Locate every blood parasite and identify its species.
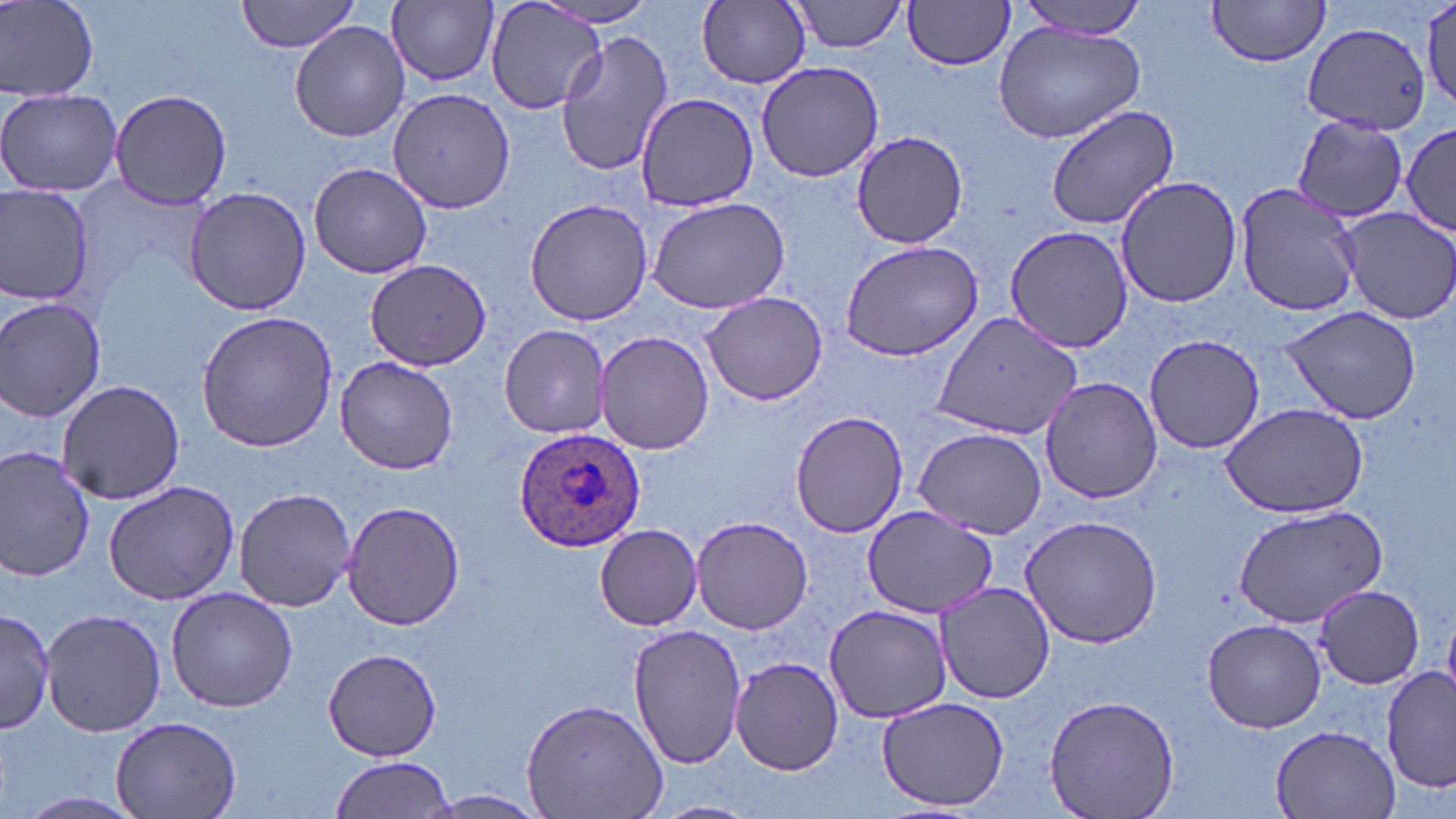
Approximate bounding boxes as named x1/y1/x2/y2 corners in pixels.
Plasmodium ovale-infected red blood cells: (x1=513, y1=426, x2=645, y2=554).
No Plasmodium falciparum, Plasmodium malariae, Plasmodium vivax, Babesia divergens, or Trypanosoma brucei observed.

Summary:
  - Uninfected red blood cell locations: (x1=2, y1=0, x2=98, y2=101), (x1=235, y1=0, x2=366, y2=54), (x1=484, y1=0, x2=607, y2=116), (x1=788, y1=0, x2=909, y2=54), (x1=903, y1=0, x2=1017, y2=71), (x1=1013, y1=0, x2=1153, y2=39), (x1=1206, y1=0, x2=1332, y2=66), (x1=388, y1=1, x2=498, y2=87), (x1=536, y1=1, x2=662, y2=29), (x1=697, y1=2, x2=810, y2=89), (x1=1421, y1=2, x2=1456, y2=110), (x1=290, y1=21, x2=410, y2=143), (x1=994, y1=21, x2=1145, y2=142), (x1=1305, y1=21, x2=1433, y2=133), (x1=554, y1=29, x2=674, y2=179), (x1=757, y1=60, x2=884, y2=184), (x1=388, y1=86, x2=515, y2=212), (x1=0, y1=87, x2=122, y2=198), (x1=108, y1=88, x2=232, y2=208), (x1=634, y1=93, x2=760, y2=211), (x1=1045, y1=103, x2=1181, y2=229), (x1=1292, y1=115, x2=1411, y2=223), (x1=1401, y1=121, x2=1454, y2=241), (x1=848, y1=130, x2=969, y2=248), (x1=307, y1=162, x2=433, y2=278), (x1=1115, y1=175, x2=1243, y2=308), (x1=1235, y1=181, x2=1363, y2=319), (x1=0, y1=183, x2=95, y2=309), (x1=184, y1=185, x2=311, y2=317), (x1=645, y1=195, x2=791, y2=315), (x1=524, y1=198, x2=654, y2=327), (x1=1337, y1=207, x2=1456, y2=324), (x1=1002, y1=224, x2=1136, y2=355), (x1=839, y1=238, x2=986, y2=361), (x1=364, y1=258, x2=491, y2=370), (x1=700, y1=290, x2=831, y2=406), (x1=0, y1=297, x2=106, y2=423), (x1=1280, y1=303, x2=1423, y2=426), (x1=196, y1=309, x2=338, y2=453), (x1=930, y1=310, x2=1082, y2=441), (x1=499, y1=324, x2=614, y2=438), (x1=596, y1=331, x2=714, y2=456), (x1=1142, y1=334, x2=1268, y2=455), (x1=336, y1=356, x2=458, y2=475), (x1=1040, y1=377, x2=1165, y2=503), (x1=57, y1=379, x2=187, y2=503), (x1=1219, y1=402, x2=1370, y2=519), (x1=789, y1=409, x2=910, y2=537), (x1=911, y1=426, x2=1048, y2=536), (x1=0, y1=445, x2=96, y2=583), (x1=103, y1=480, x2=243, y2=606), (x1=232, y1=487, x2=359, y2=612), (x1=340, y1=500, x2=467, y2=631), (x1=1234, y1=505, x2=1388, y2=628), (x1=862, y1=507, x2=997, y2=619), (x1=1016, y1=514, x2=1163, y2=649), (x1=691, y1=515, x2=813, y2=635), (x1=594, y1=524, x2=702, y2=630), (x1=934, y1=579, x2=1056, y2=703), (x1=1317, y1=584, x2=1426, y2=690), (x1=166, y1=587, x2=298, y2=714), (x1=824, y1=606, x2=952, y2=722), (x1=41, y1=607, x2=165, y2=736), (x1=0, y1=610, x2=57, y2=734), (x1=1203, y1=618, x2=1326, y2=733), (x1=629, y1=625, x2=747, y2=770), (x1=323, y1=649, x2=442, y2=760), (x1=730, y1=657, x2=843, y2=775), (x1=1382, y1=667, x2=1455, y2=794), (x1=1044, y1=694, x2=1179, y2=819), (x1=876, y1=696, x2=1010, y2=812), (x1=520, y1=697, x2=669, y2=819), (x1=111, y1=714, x2=241, y2=819), (x1=1268, y1=723, x2=1404, y2=817), (x1=328, y1=755, x2=456, y2=819), (x1=423, y1=790, x2=546, y2=816), (x1=18, y1=791, x2=144, y2=816), (x1=647, y1=800, x2=761, y2=819)
  - Slide-level diagnosis: Plasmodium ovale
  - Stain: May-Grünwald-Giemsa
  - Image size: 1456×819 pixels
  - Field of view: single
  - Modality: optical microscopy
  - Preparation: thin blood smear
  - Magnification: 1000x